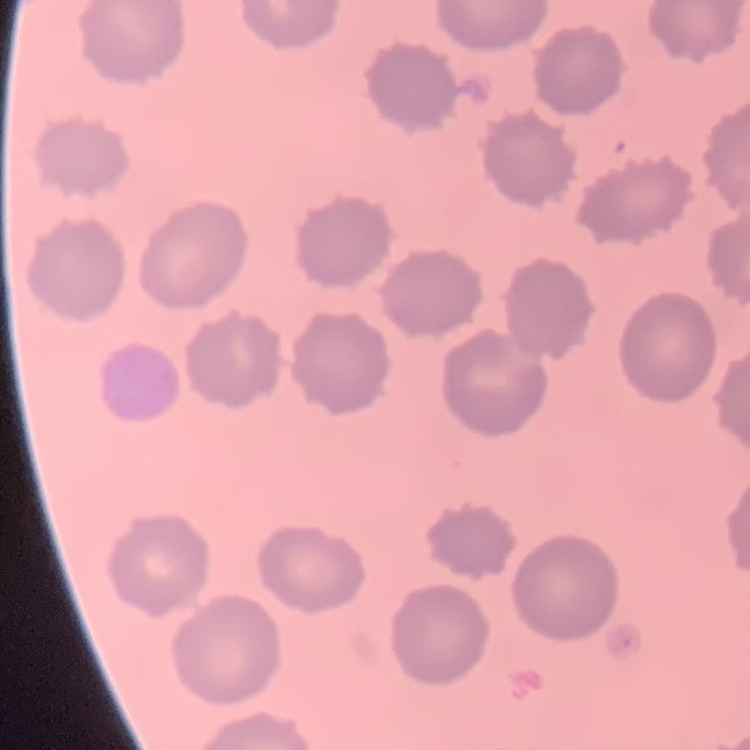

Summary:
  - Red blood cell morphology: no rouleaux formation
  - Preparation: thin blood film
  - Image type: square crop of a larger photomicrograph
  - Stain: Field's or Giemsa